Describe the morphology of the erythrocytes.
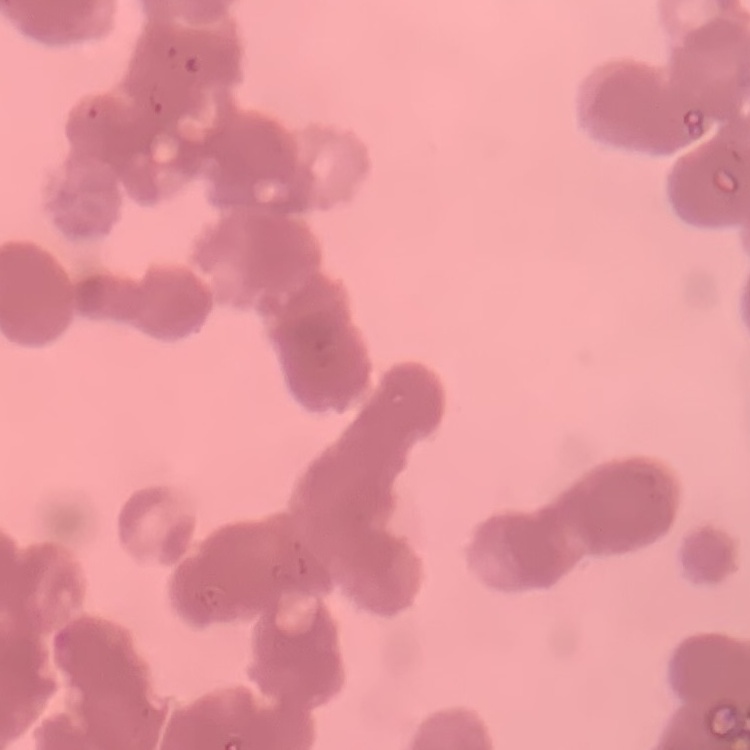
Rouleaux formation.

Thin blood smear. One tile cut from a larger photomicrograph. Stained with either Field's or Giemsa.